Report the malaria status of this cell.
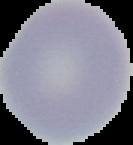

Uninfected.

image_size: 133×145 pixels
preparation: thin blood smear
image_type: segmented cell region with the area outside set to black